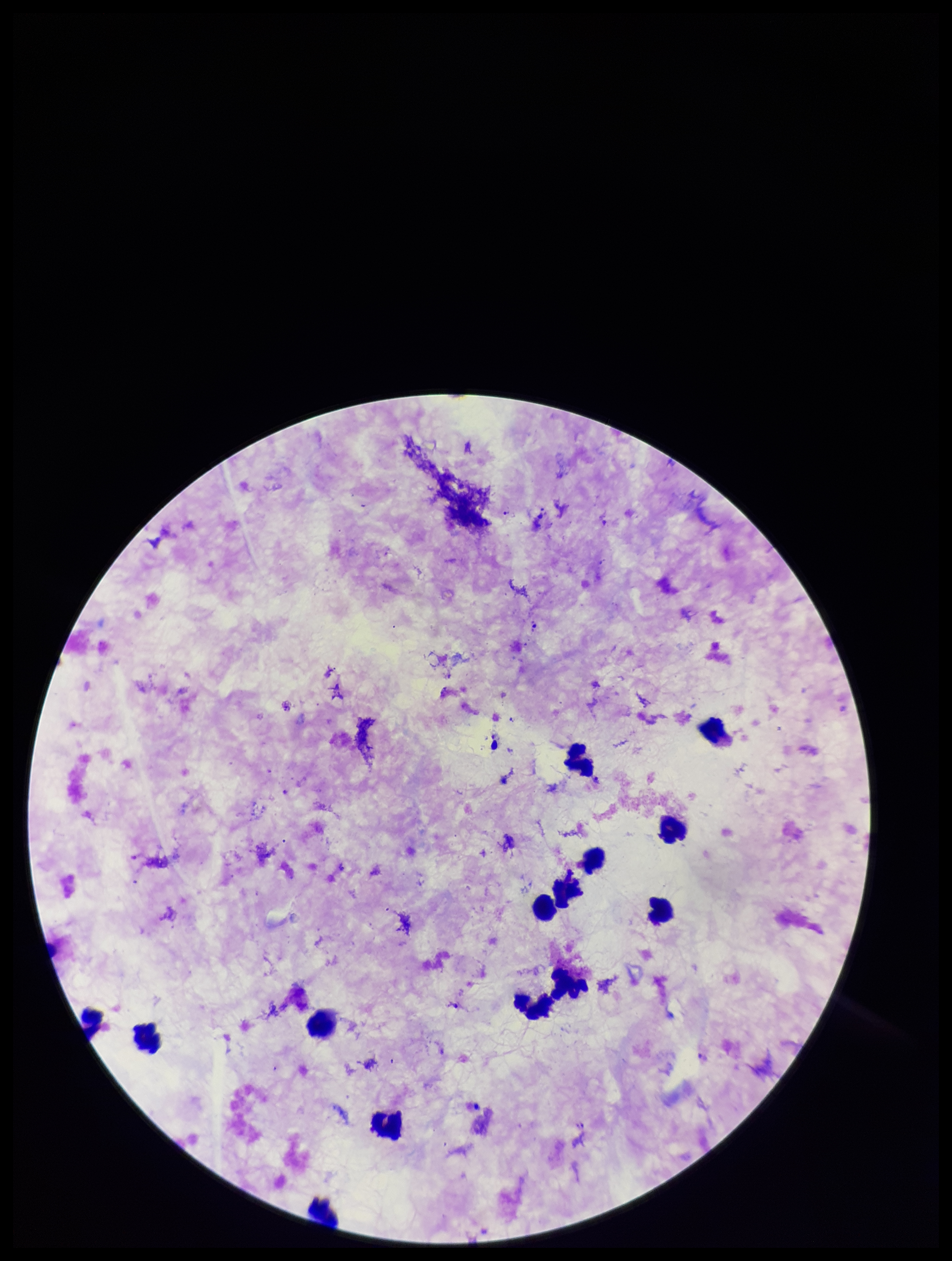

{
  "image_size": "952×1261 pixels",
  "field_of_view": "single",
  "plasmodium_parasites": "identified",
  "stain": "Giemsa",
  "preparation": "thick",
  "parasite_count": 4,
  "species_reported_for_this_patient": "Plasmodium falciparum",
  "leukocyte_count": 13,
  "capture": "smartphone photograph through the microscope eyepiece",
  "patient_malaria_status": "positive"
}